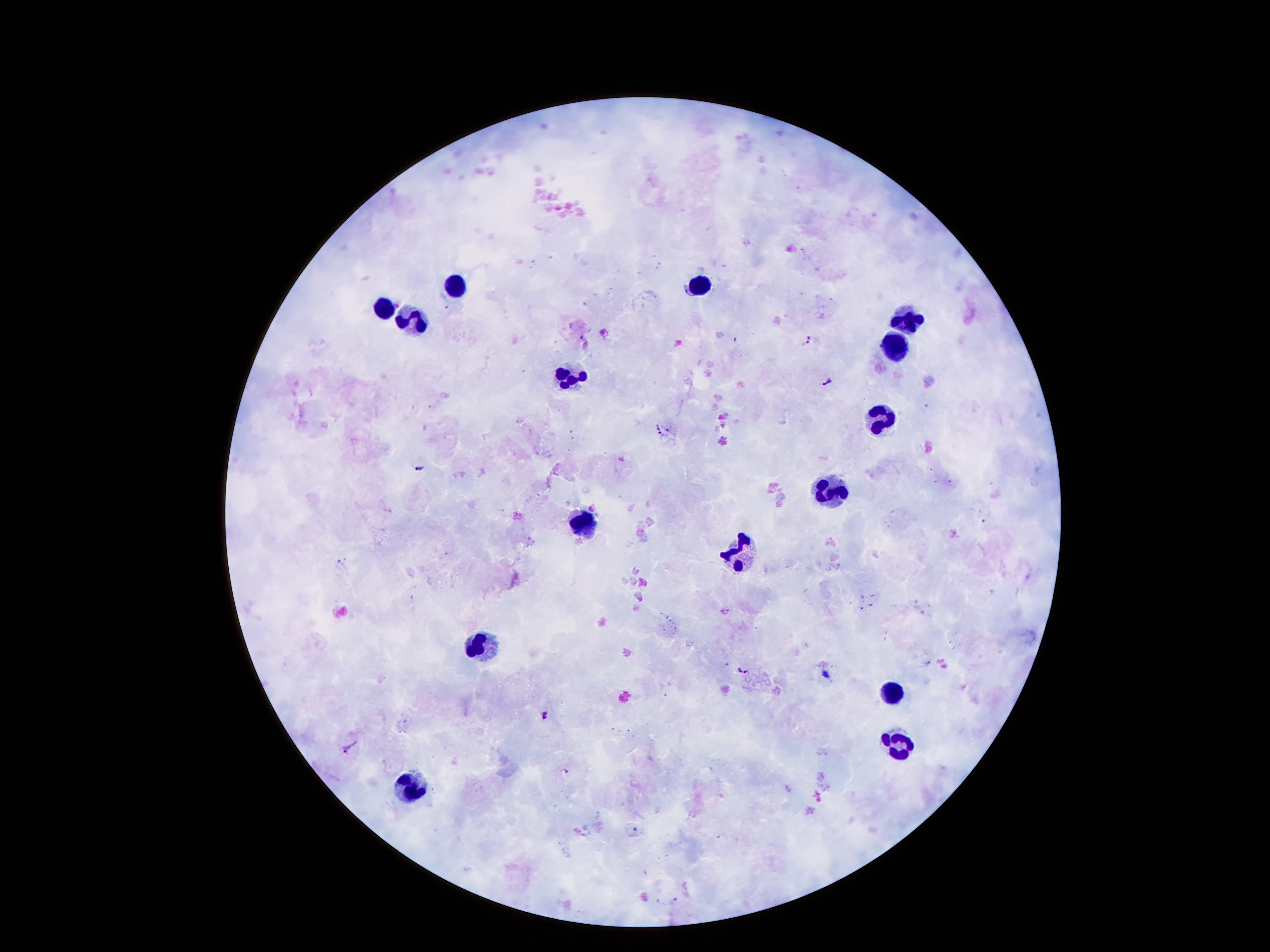
coordinate format = approximate centers as {x, y} in pixels
Plasmodium parasite locations = {809, 341}, {827, 379}, {659, 430}, {421, 467}, {743, 671}, {828, 675}, {543, 716}, {349, 747}
leukocyte locations = {456, 282}, {701, 283}, {383, 307}, {417, 319}, {906, 323}, {898, 343}, {570, 374}, {881, 420}, {831, 489}, {582, 521}, {741, 552}, {483, 644}, {892, 693}, {898, 744}, {411, 782}
field of view = single
image size = 1270×952 pixels
patient malaria status = infected with Plasmodium falciparum
capture = smartphone camera through the microscope eyepiece
stain = Giemsa
preparation = thick peripheral-blood smear
magnification = 100x